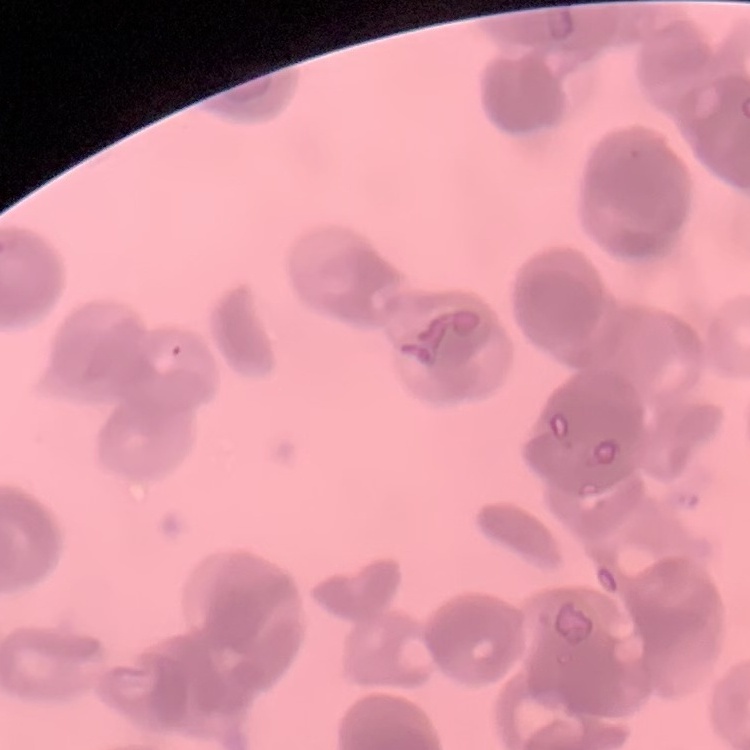
The red blood cells exhibit rouleaux formation. Thin peripheral smear. Square crop of a larger photomicrograph. Stained with either Field's or Giemsa.